Outline every parasitised red blood cell.
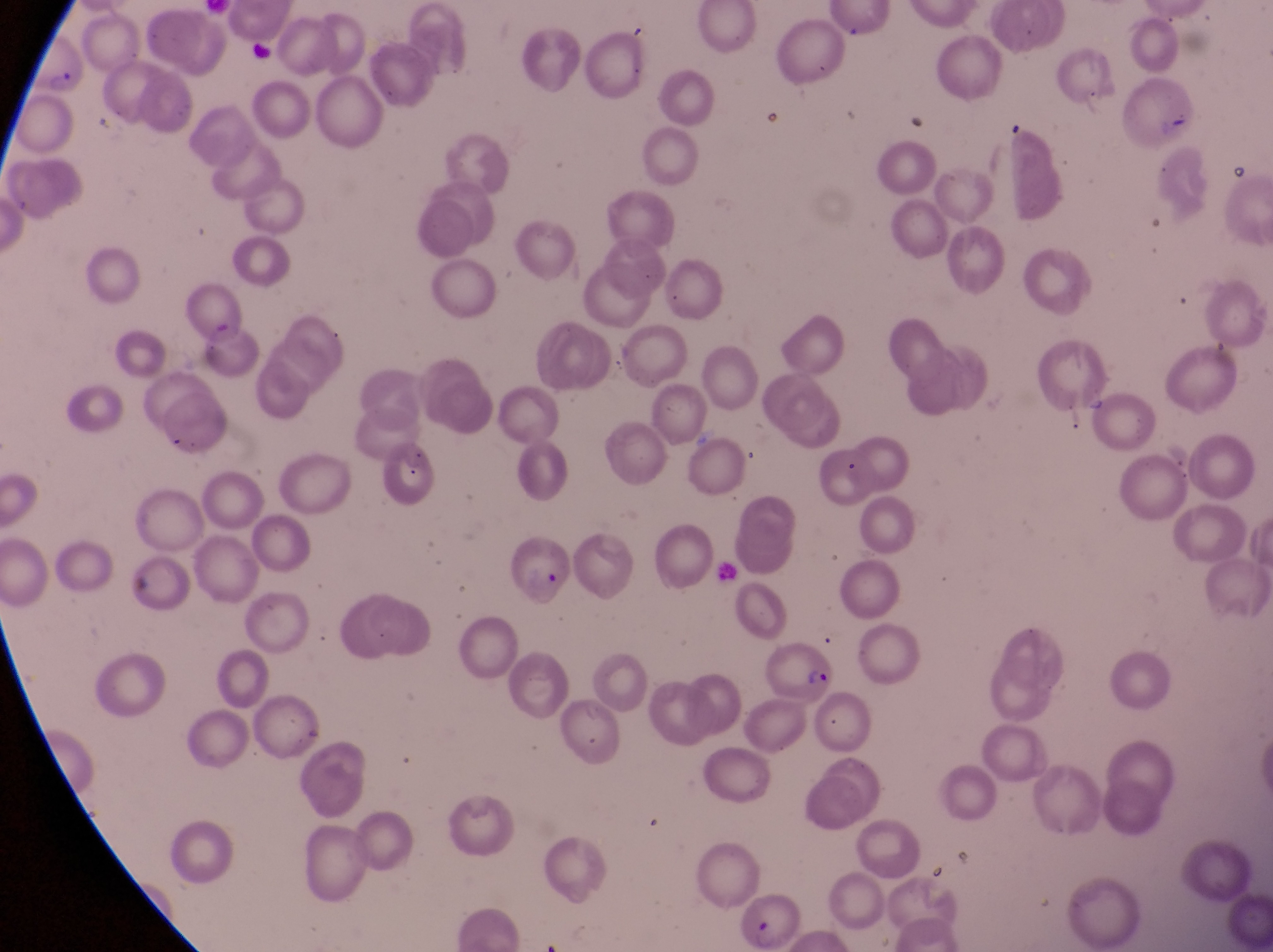

Approximate bounding boxes as (left, top, right, bottom) in pixels.
Parasitised red blood cells: (30, 40, 87, 98), (512, 534, 577, 612), (773, 632, 838, 702), (724, 889, 802, 949).

field of view = single
image size = 1273×952 pixels
capture = smartphone photograph through the eyepiece of an Olympus CX-23 microscope
preparation = thin blood film
magnification = 1000x
country = Uganda